Classify this cell by malaria status.
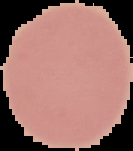
Uninfected.

image_size: 133×151 pixels
preparation: thin blood film
image_type: segmented cell region on a black background